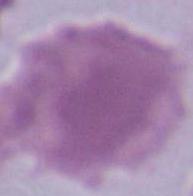

magnification: 1000x
identification: red blood cell
modality: micrograph